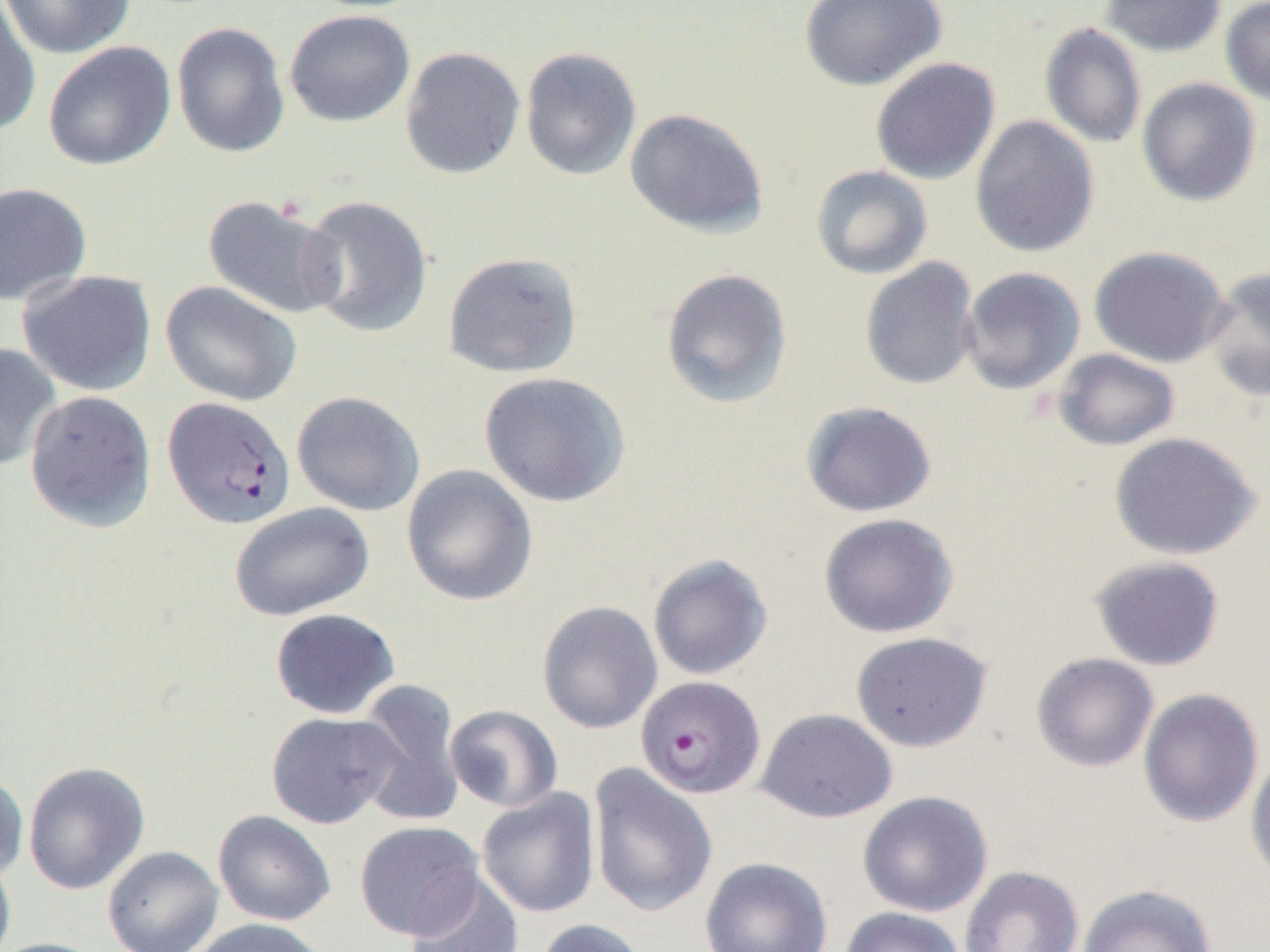
Summary:
  - Coordinate format: approximate bounding boxes as (x1, y1, x2, y2) in pixels
  - Uninfected red blood cell locations: (1, 0, 135, 59), (798, 0, 947, 91), (1102, 0, 1226, 56), (1220, 0, 1270, 107), (0, 3, 42, 137), (284, 10, 415, 127), (172, 22, 290, 158), (1041, 23, 1147, 149), (43, 41, 176, 171), (400, 46, 525, 179), (519, 47, 642, 181), (871, 57, 1000, 185), (1137, 78, 1261, 206), (625, 108, 769, 238), (970, 115, 1100, 257), (810, 165, 933, 280), (0, 182, 92, 306), (203, 195, 344, 320), (298, 195, 433, 338), (1089, 246, 1232, 367), (443, 251, 583, 378), (859, 257, 980, 391), (1202, 266, 1270, 404), (959, 267, 1086, 395), (661, 268, 793, 409), (18, 270, 157, 396), (160, 280, 303, 407), (0, 342, 61, 472), (1052, 348, 1180, 451), (478, 371, 632, 507), (24, 390, 156, 532), (291, 391, 425, 516), (800, 401, 937, 518), (1108, 431, 1261, 560), (401, 464, 538, 607), (229, 502, 374, 621), (819, 513, 959, 638), (647, 554, 773, 681), (1089, 555, 1225, 671), (536, 600, 662, 734), (270, 608, 400, 719), (851, 631, 993, 752), (1031, 652, 1159, 772), (354, 679, 467, 828), (1138, 688, 1264, 828), (444, 705, 563, 812), (755, 708, 898, 823), (266, 711, 401, 829), (1245, 749, 1270, 885), (22, 761, 150, 895), (588, 763, 718, 918), (0, 770, 29, 882), (477, 789, 600, 917), (857, 790, 992, 917), (212, 810, 337, 926), (354, 820, 485, 942), (102, 845, 224, 952), (0, 851, 17, 952), (700, 857, 832, 952), (959, 865, 1085, 952), (405, 874, 523, 952), (1078, 884, 1218, 952), (838, 906, 966, 952), (187, 918, 330, 952), (534, 918, 650, 952), (0, 937, 108, 952)
  - Plasmodium falciparum-infected red blood cell locations: (162, 396, 296, 529), (635, 675, 765, 799)
  - Slide-level diagnosis: Plasmodium falciparum
  - Magnification: 1000x
  - Preparation: thin blood smear
  - Image size: 1270×952 pixels
  - Field of view: one of a larger specimen
  - Modality: optical microscopy